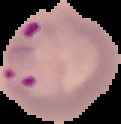

Summary:
  - Preparation: thin blood film
  - Image size: 121×124 pixels
  - Result: malaria parasites identified
  - Image type: segmented cell region on a black background